Locate every uninfected red blood cell.
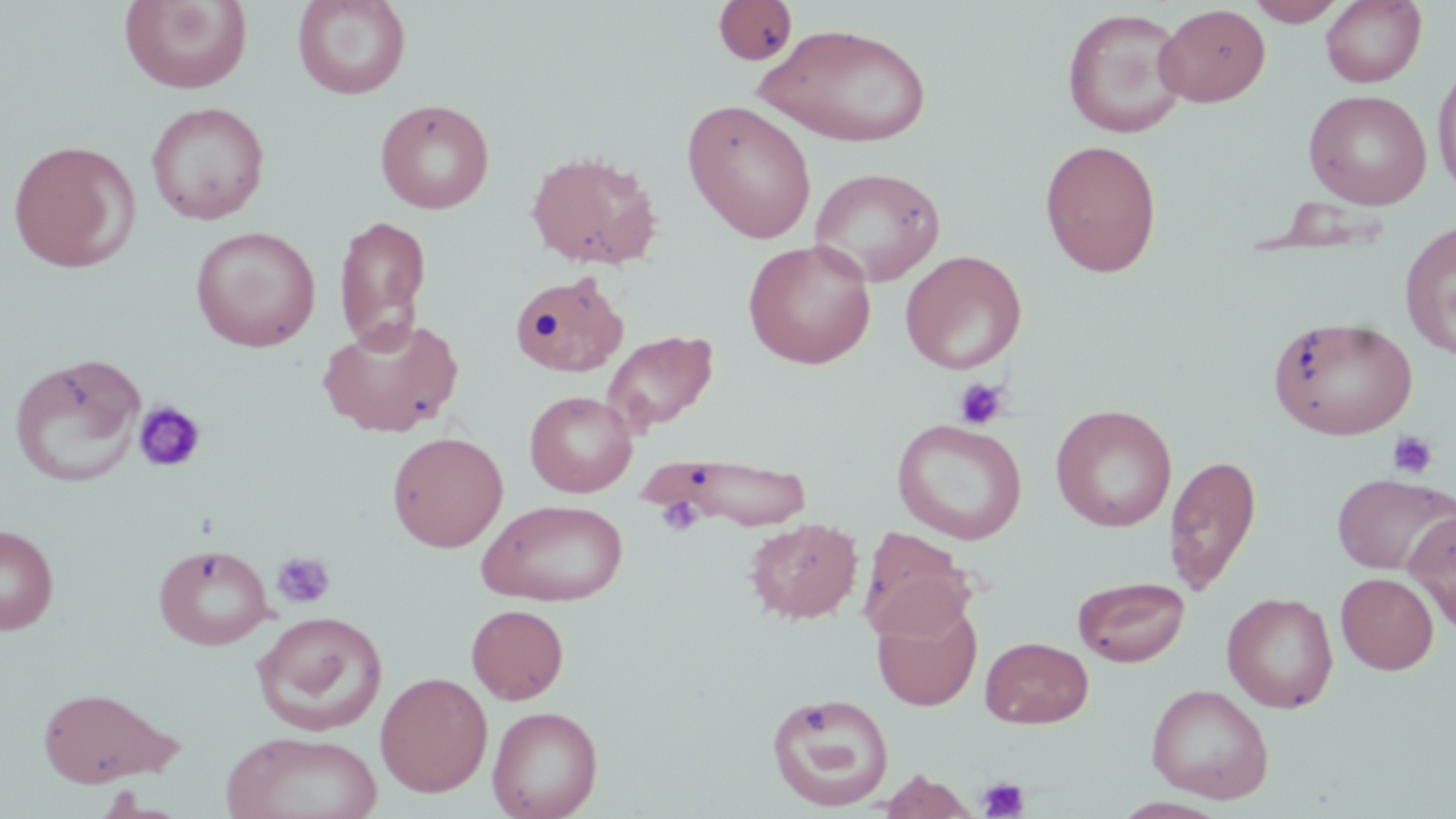
Approximate bounding boxes as (x1,y1)-(x2,y2) corner pairs in pixels.
Uninfected red blood cells: (292,0)-(411,99), (1245,0)-(1348,26), (1321,0)-(1426,87), (119,1)-(252,93), (712,1)-(799,64), (1155,4)-(1271,107), (1061,8)-(1190,139), (755,23)-(933,148), (1433,60)-(1456,199), (1303,88)-(1432,209), (375,98)-(496,214), (682,99)-(817,243), (145,101)-(270,225), (1040,139)-(1162,278), (7,140)-(140,273), (526,150)-(662,270), (809,166)-(945,287), (332,214)-(432,348), (1399,220)-(1456,359), (190,226)-(321,352), (743,239)-(877,369), (900,250)-(1027,374), (507,270)-(637,376), (318,315)-(465,437), (1267,315)-(1418,439), (602,329)-(719,434), (9,353)-(147,488), (525,390)-(637,497), (1050,405)-(1177,531), (891,418)-(1028,545), (387,431)-(508,553), (619,452)-(817,531), (1164,453)-(1262,594), (1332,472)-(1454,575), (477,499)-(628,606), (1403,508)-(1456,630), (744,518)-(862,624), (0,524)-(59,635), (858,528)-(979,640), (153,543)-(275,650), (1336,572)-(1439,674), (1073,576)-(1190,667), (1222,592)-(1339,713), (872,602)-(982,712), (466,604)-(569,705), (251,611)-(389,736), (980,636)-(1094,728), (374,671)-(493,798), (1146,683)-(1274,804), (37,686)-(179,787), (766,693)-(896,812), (487,705)-(603,819), (221,731)-(383,819), (878,769)-(978,818).

Platelet locations: (954,377)-(1010,430), (133,401)-(206,474), (1385,429)-(1439,481), (654,492)-(706,538), (271,551)-(336,610), (977,777)-(1030,819). Slide-level diagnosis: negative for blood parasites. One field of a larger specimen. Image is 1456×819 pixels. Optical microscopy. Thin blood smear. May-Grünwald-Giemsa-stained preparation. 1000x magnification.